Give the position of every Plasmodium parasite visible.
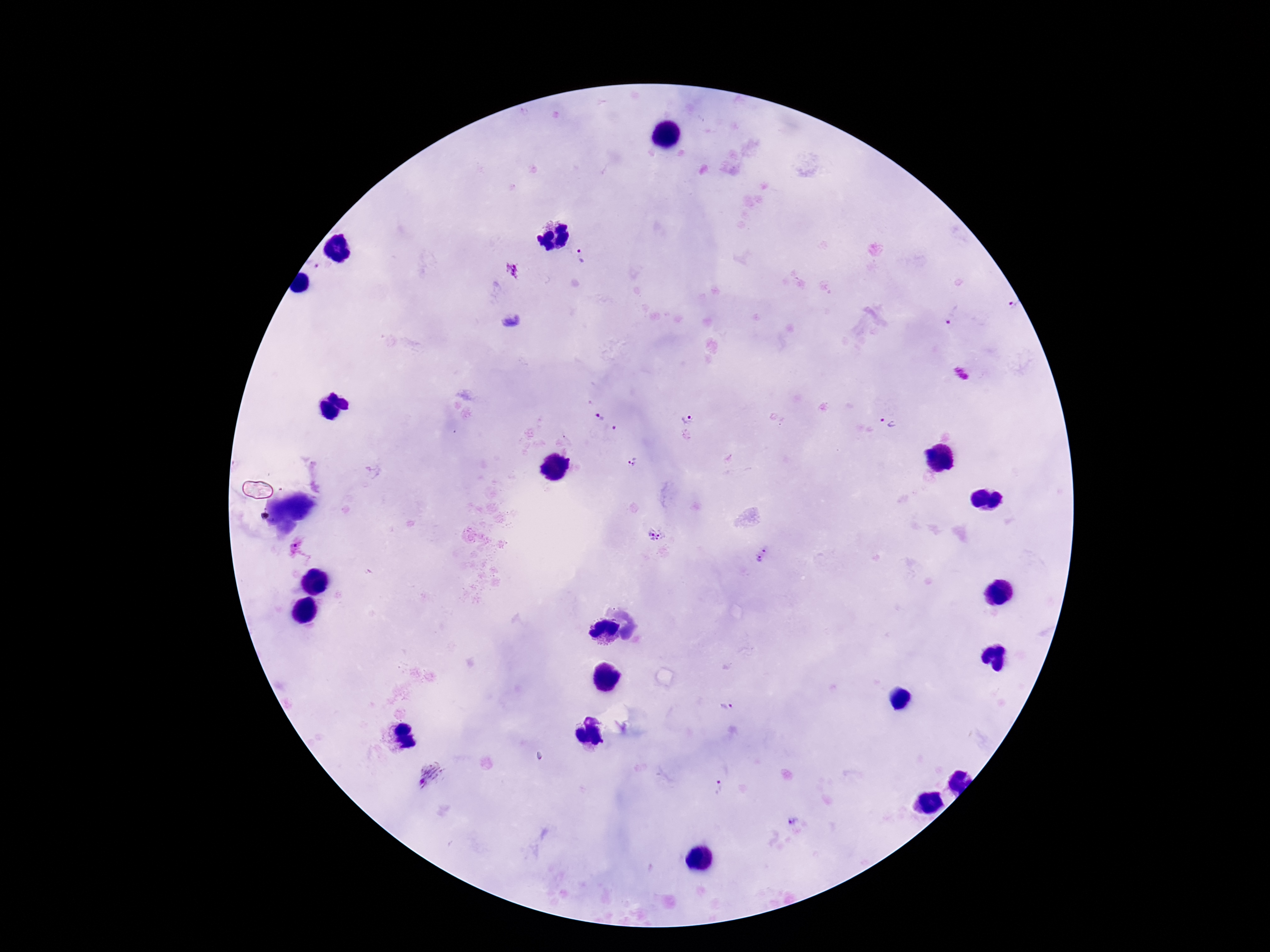
Approximate centers as (x, y) in pixels.
Plasmodium parasites: (580, 257), (314, 265), (1010, 308), (953, 316), (510, 321), (964, 374), (687, 416), (599, 418), (886, 423), (616, 431), (633, 463), (657, 535), (763, 555), (726, 707), (429, 774), (718, 787), (791, 819).

{
  "patient_malaria_status": "positive",
  "magnification": "100x",
  "capture": "smartphone camera through the microscope eyepiece",
  "preparation": "thick blood film",
  "field_of_view": "single",
  "image_size": "1270×952 pixels",
  "stain": "Giemsa"
}